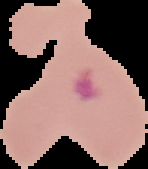
Summary:
  - Image type: cell region segmented out of the field of view; surrounding area masked to black
  - Preparation: thin blood film
  - Malaria status: parasitized
  - Image size: 148×169 pixels